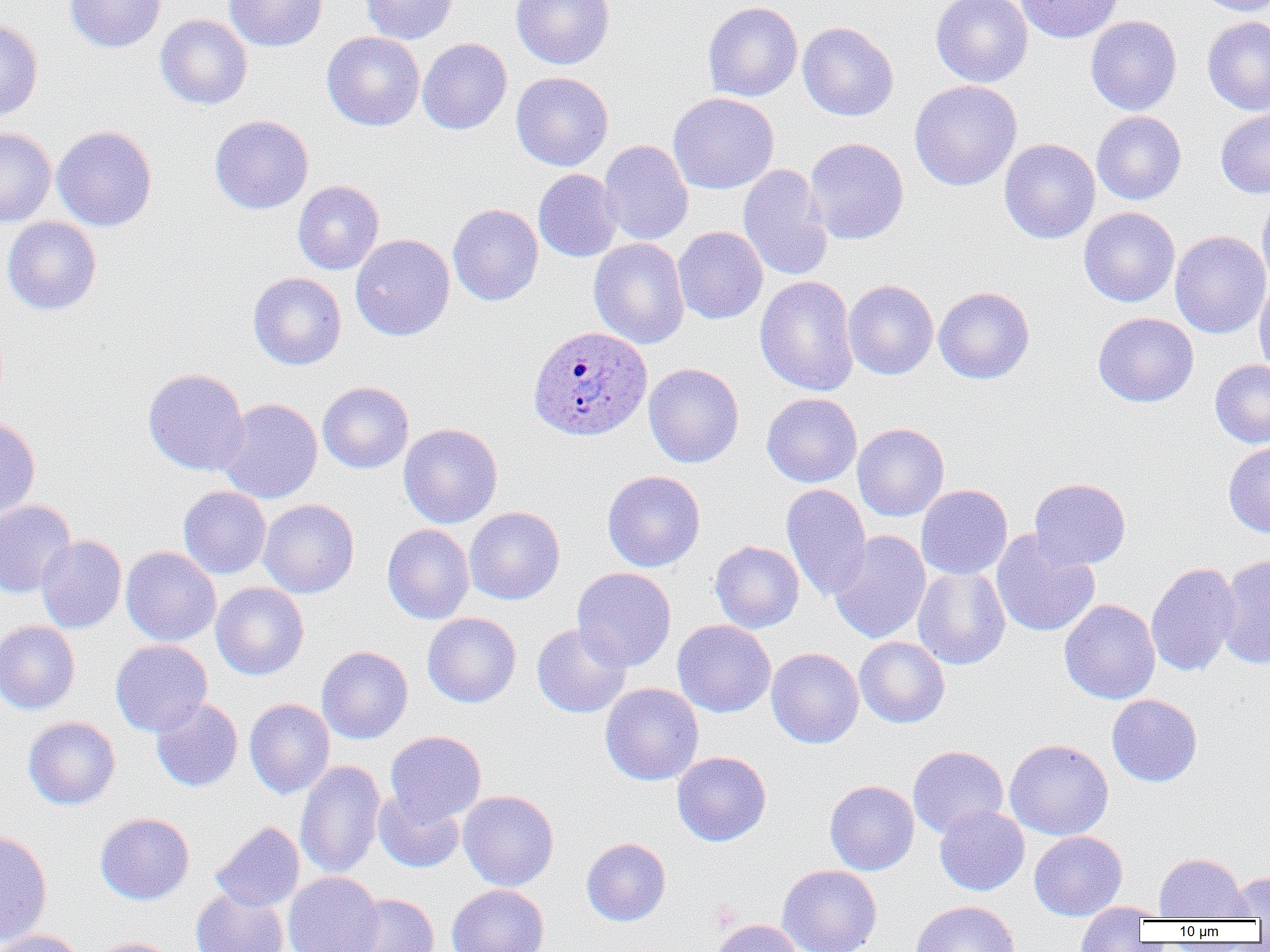
{
  "slide_level_diagnosis": "Plasmodium ovale",
  "magnification": "1000x",
  "field_of_view": "single",
  "plasmodium_ovale_infected_red_blood_cell_locations": "approximate bounding boxes as named x1/y1/x2/y2 corners in pixels: (x1=527, y1=325, x2=652, y2=442)",
  "platelet_locations": "approximate bounding boxes as named x1/y1/x2/y2 corners in pixels: (x1=710, y1=900, x2=741, y2=930)",
  "modality": "light microscopy",
  "image_size": "1270×952 pixels",
  "preparation": "thin blood smear",
  "uninfected_red_blood_cell_locations": "approximate bounding boxes as named x1/y1/x2/y2 corners in pixels: (x1=64, y1=0, x2=166, y2=53), (x1=224, y1=0, x2=328, y2=52), (x1=360, y1=0, x2=459, y2=44), (x1=511, y1=0, x2=615, y2=69), (x1=931, y1=0, x2=1033, y2=87), (x1=1016, y1=0, x2=1124, y2=43), (x1=1195, y1=0, x2=1270, y2=16), (x1=703, y1=2, x2=803, y2=102), (x1=155, y1=15, x2=252, y2=109), (x1=1085, y1=15, x2=1182, y2=116), (x1=1203, y1=16, x2=1270, y2=115), (x1=0, y1=19, x2=43, y2=122), (x1=798, y1=21, x2=899, y2=121), (x1=322, y1=32, x2=424, y2=130), (x1=417, y1=37, x2=512, y2=135), (x1=511, y1=72, x2=613, y2=171), (x1=909, y1=80, x2=1022, y2=191), (x1=668, y1=93, x2=779, y2=194), (x1=1216, y1=108, x2=1270, y2=198), (x1=1091, y1=110, x2=1186, y2=205), (x1=209, y1=115, x2=313, y2=214), (x1=51, y1=125, x2=157, y2=232), (x1=0, y1=128, x2=56, y2=228), (x1=804, y1=137, x2=909, y2=246), (x1=999, y1=138, x2=1100, y2=244), (x1=598, y1=140, x2=693, y2=246), (x1=738, y1=164, x2=834, y2=281), (x1=534, y1=169, x2=623, y2=262), (x1=293, y1=181, x2=384, y2=274), (x1=1257, y1=191, x2=1270, y2=294), (x1=447, y1=203, x2=544, y2=306), (x1=1079, y1=207, x2=1180, y2=307), (x1=2, y1=217, x2=102, y2=315), (x1=1079, y1=218, x2=1269, y2=317), (x1=673, y1=226, x2=768, y2=324), (x1=1169, y1=230, x2=1270, y2=339), (x1=350, y1=233, x2=455, y2=341), (x1=589, y1=238, x2=690, y2=349), (x1=248, y1=272, x2=346, y2=370), (x1=755, y1=275, x2=859, y2=397), (x1=1253, y1=278, x2=1270, y2=382), (x1=843, y1=280, x2=938, y2=380), (x1=933, y1=286, x2=1035, y2=384), (x1=1092, y1=312, x2=1199, y2=407), (x1=1210, y1=359, x2=1270, y2=448), (x1=643, y1=363, x2=744, y2=468), (x1=143, y1=368, x2=250, y2=476), (x1=317, y1=381, x2=413, y2=473), (x1=762, y1=392, x2=862, y2=487), (x1=217, y1=398, x2=323, y2=504), (x1=0, y1=416, x2=40, y2=519), (x1=852, y1=422, x2=949, y2=522), (x1=398, y1=423, x2=503, y2=528), (x1=1223, y1=441, x2=1270, y2=538), (x1=602, y1=470, x2=705, y2=572), (x1=1029, y1=477, x2=1131, y2=569), (x1=781, y1=483, x2=872, y2=602), (x1=916, y1=484, x2=1012, y2=579), (x1=178, y1=486, x2=271, y2=579), (x1=258, y1=499, x2=359, y2=598), (x1=0, y1=500, x2=76, y2=598), (x1=464, y1=506, x2=564, y2=605), (x1=382, y1=524, x2=474, y2=624), (x1=829, y1=530, x2=931, y2=644), (x1=991, y1=530, x2=1100, y2=637), (x1=36, y1=535, x2=126, y2=633), (x1=710, y1=541, x2=804, y2=633), (x1=120, y1=546, x2=221, y2=646), (x1=1217, y1=555, x2=1270, y2=669), (x1=1145, y1=562, x2=1242, y2=677), (x1=912, y1=566, x2=1010, y2=670), (x1=571, y1=567, x2=676, y2=671), (x1=211, y1=582, x2=309, y2=680), (x1=1059, y1=599, x2=1160, y2=704), (x1=422, y1=613, x2=521, y2=708), (x1=672, y1=619, x2=776, y2=717), (x1=0, y1=620, x2=80, y2=715), (x1=531, y1=623, x2=632, y2=718), (x1=854, y1=637, x2=950, y2=728), (x1=110, y1=639, x2=212, y2=737), (x1=316, y1=645, x2=413, y2=744), (x1=766, y1=647, x2=864, y2=748), (x1=599, y1=683, x2=703, y2=786), (x1=1106, y1=694, x2=1203, y2=787), (x1=150, y1=698, x2=243, y2=792), (x1=244, y1=698, x2=334, y2=799), (x1=23, y1=716, x2=120, y2=810), (x1=385, y1=730, x2=486, y2=825), (x1=1004, y1=739, x2=1114, y2=840), (x1=908, y1=745, x2=1008, y2=838), (x1=672, y1=751, x2=771, y2=846), (x1=295, y1=759, x2=386, y2=879), (x1=824, y1=780, x2=919, y2=875), (x1=373, y1=790, x2=465, y2=873), (x1=458, y1=790, x2=559, y2=891), (x1=934, y1=805, x2=1029, y2=896), (x1=95, y1=812, x2=194, y2=905), (x1=210, y1=821, x2=305, y2=912), (x1=0, y1=830, x2=53, y2=947), (x1=1029, y1=831, x2=1127, y2=920), (x1=581, y1=838, x2=671, y2=926), (x1=1154, y1=853, x2=1250, y2=921), (x1=777, y1=864, x2=882, y2=952), (x1=1224, y1=870, x2=1270, y2=920), (x1=283, y1=872, x2=383, y2=952), (x1=447, y1=884, x2=549, y2=952), (x1=190, y1=889, x2=289, y2=952), (x1=344, y1=893, x2=440, y2=952), (x1=910, y1=900, x2=1020, y2=952), (x1=1075, y1=904, x2=1153, y2=951), (x1=711, y1=919, x2=803, y2=952), (x1=0, y1=929, x2=86, y2=952), (x1=85, y1=936, x2=181, y2=952)"
}